Assess this cell for malaria.
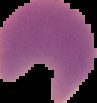

It is parasitized.

The area outside the segmented cell region is set to black. Image is 97×103 pixels. From a thin blood film.